Locate every blood parasite and identify its species.
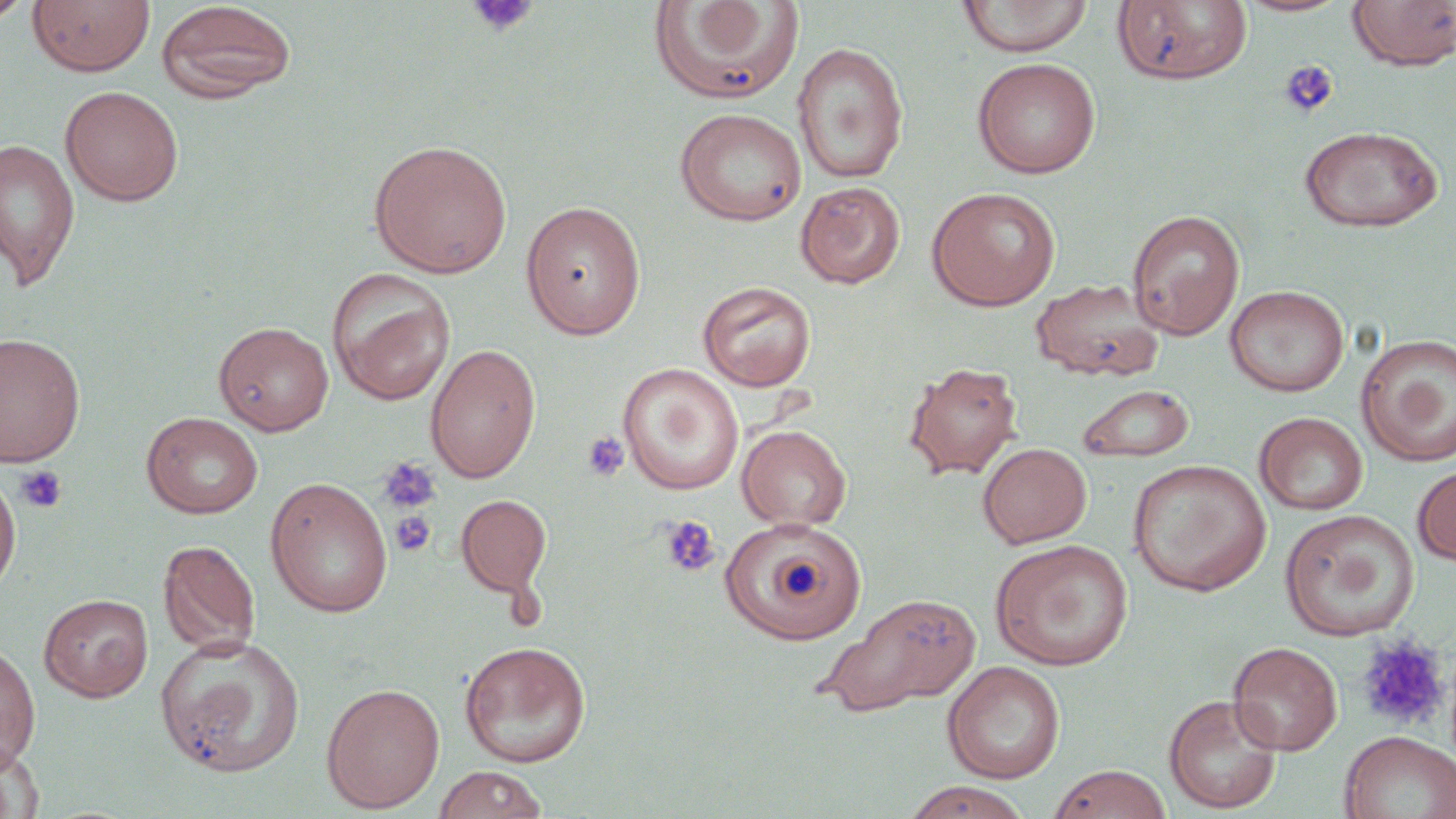

No blood parasites observed.

Summary:
  - Coordinate format: approximate bounding boxes as named x1/y1/x2/y2 corners in pixels
  - Platelet locations: (x1=466, y1=0, x2=539, y2=38), (x1=1279, y1=60, x2=1339, y2=119), (x1=582, y1=432, x2=630, y2=481), (x1=377, y1=455, x2=441, y2=514), (x1=15, y1=466, x2=67, y2=514), (x1=390, y1=511, x2=436, y2=557), (x1=660, y1=515, x2=722, y2=578), (x1=1356, y1=636, x2=1449, y2=730)
  - Uninfected red blood cell locations: (x1=0, y1=0, x2=31, y2=26), (x1=26, y1=0, x2=155, y2=77), (x1=956, y1=0, x2=1093, y2=58), (x1=1235, y1=0, x2=1352, y2=18), (x1=649, y1=1, x2=804, y2=104), (x1=1112, y1=1, x2=1253, y2=84), (x1=1346, y1=1, x2=1456, y2=72), (x1=155, y1=2, x2=298, y2=104), (x1=791, y1=42, x2=909, y2=184), (x1=972, y1=58, x2=1101, y2=177), (x1=59, y1=85, x2=184, y2=206), (x1=674, y1=107, x2=807, y2=226), (x1=1298, y1=125, x2=1444, y2=233), (x1=368, y1=138, x2=512, y2=278), (x1=0, y1=139, x2=80, y2=291), (x1=796, y1=181, x2=905, y2=289), (x1=927, y1=187, x2=1060, y2=311), (x1=519, y1=200, x2=647, y2=340), (x1=1127, y1=209, x2=1245, y2=340), (x1=327, y1=268, x2=455, y2=406), (x1=1030, y1=278, x2=1165, y2=382), (x1=697, y1=281, x2=817, y2=392), (x1=1225, y1=285, x2=1349, y2=397), (x1=213, y1=321, x2=334, y2=436), (x1=0, y1=332, x2=86, y2=468), (x1=1355, y1=333, x2=1456, y2=468), (x1=425, y1=343, x2=541, y2=484), (x1=903, y1=361, x2=1023, y2=481), (x1=617, y1=363, x2=744, y2=495), (x1=1077, y1=384, x2=1195, y2=463), (x1=141, y1=411, x2=263, y2=519), (x1=1254, y1=412, x2=1369, y2=515), (x1=737, y1=424, x2=851, y2=531), (x1=977, y1=442, x2=1092, y2=548), (x1=1128, y1=459, x2=1272, y2=596), (x1=1413, y1=464, x2=1456, y2=566), (x1=0, y1=467, x2=22, y2=600), (x1=264, y1=476, x2=394, y2=618), (x1=456, y1=494, x2=552, y2=598), (x1=1279, y1=509, x2=1420, y2=641), (x1=723, y1=516, x2=863, y2=644), (x1=157, y1=539, x2=261, y2=657), (x1=990, y1=539, x2=1134, y2=671), (x1=816, y1=591, x2=981, y2=717), (x1=39, y1=594, x2=153, y2=702), (x1=154, y1=634, x2=306, y2=778), (x1=459, y1=640, x2=592, y2=767), (x1=0, y1=641, x2=40, y2=772), (x1=1228, y1=641, x2=1343, y2=755), (x1=941, y1=661, x2=1066, y2=783), (x1=321, y1=682, x2=445, y2=813), (x1=1163, y1=693, x2=1283, y2=814), (x1=1339, y1=730, x2=1456, y2=819), (x1=0, y1=739, x2=42, y2=818), (x1=1048, y1=764, x2=1173, y2=819), (x1=432, y1=765, x2=550, y2=818), (x1=900, y1=780, x2=1035, y2=819)
  - Slide-level diagnosis: no evidence of blood parasites
  - Image size: 1456×819 pixels
  - Field of view: one of a larger specimen
  - Stain: May-Grünwald-Giemsa
  - Modality: optical microscopy
  - Magnification: 1000x
  - Preparation: thin blood film